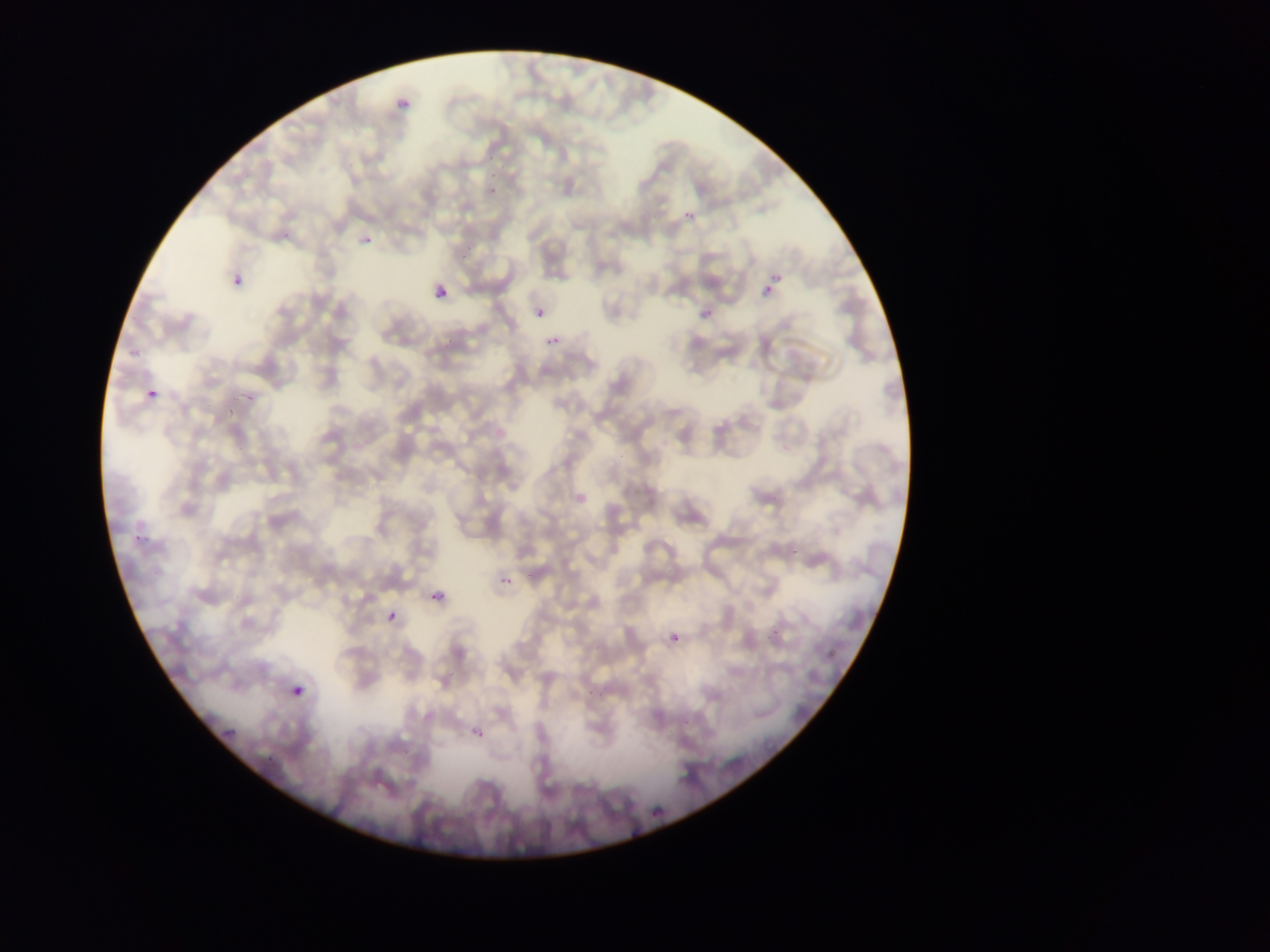

{
  "country": "Ghana",
  "field_of_view": "single",
  "image_size": "1270×952 pixels",
  "plasmodium_parasite_locations": "approximate bounding boxes as (left, top, right, bottom) in pixels: (391, 102, 415, 117), (489, 187, 499, 198), (685, 212, 695, 221), (361, 231, 374, 254), (233, 270, 253, 290), (770, 272, 784, 285), (761, 286, 772, 298), (431, 291, 450, 315), (694, 307, 712, 325), (535, 309, 544, 319), (543, 331, 569, 349), (147, 388, 158, 398), (133, 525, 152, 546), (502, 576, 514, 587), (426, 588, 452, 605), (388, 610, 397, 621), (671, 633, 680, 641), (293, 678, 310, 699), (468, 720, 491, 741), (219, 722, 242, 743), (650, 807, 663, 821)",
  "preparation": "thin blood film",
  "capture": "mobile-phone photograph through a microscope"
}